Report the malaria status of this cell.
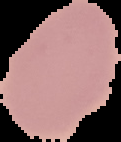

It is uninfected.

image type = segmented cell region with the area outside set to black
image size = 121×142 pixels
preparation = thin blood smear